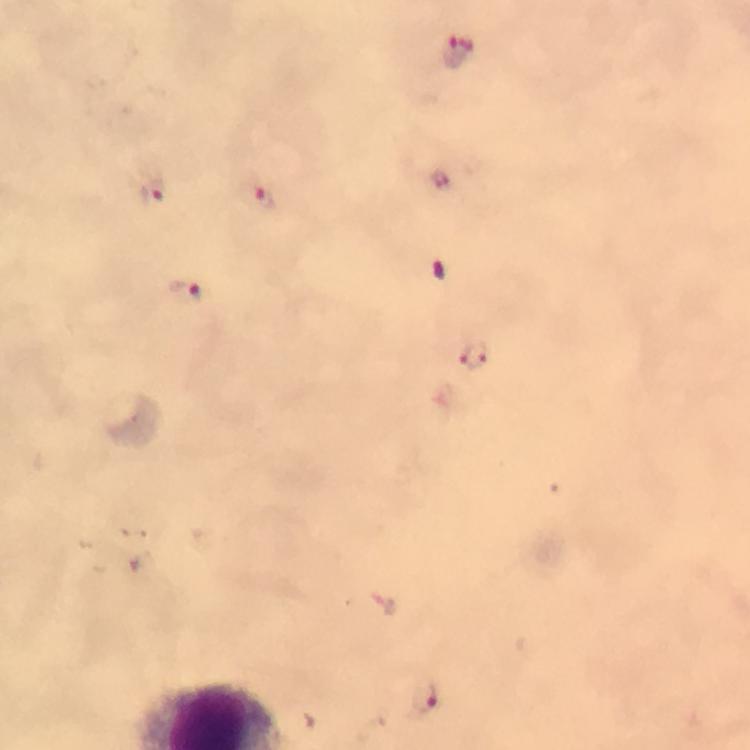
Approximate centers as {x, y} in pixels.
Summary:
  - Malaria parasite locations: {457, 52}, {153, 191}, {264, 197}, {184, 292}, {473, 357}, {384, 604}, {426, 698}
  - Capture: smartphone mounted on the microscope
  - Immersion oil: applied
  - Preparation: thick blood film
  - Stain: Giemsa
  - Magnification: 100x
  - Image size: 750×750 pixels
  - Context: from a malaria diagnostic workup
  - Cropped from: one field of view